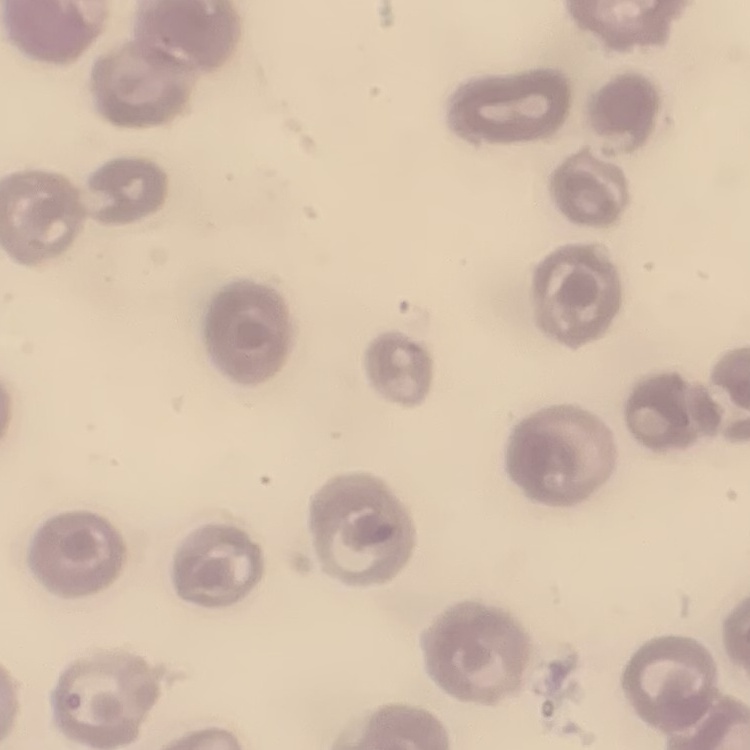
red blood cell morphology = no rouleaux formation
image type = square crop of a larger photomicrograph
preparation = thin blood smear
stain = Field's or Giemsa